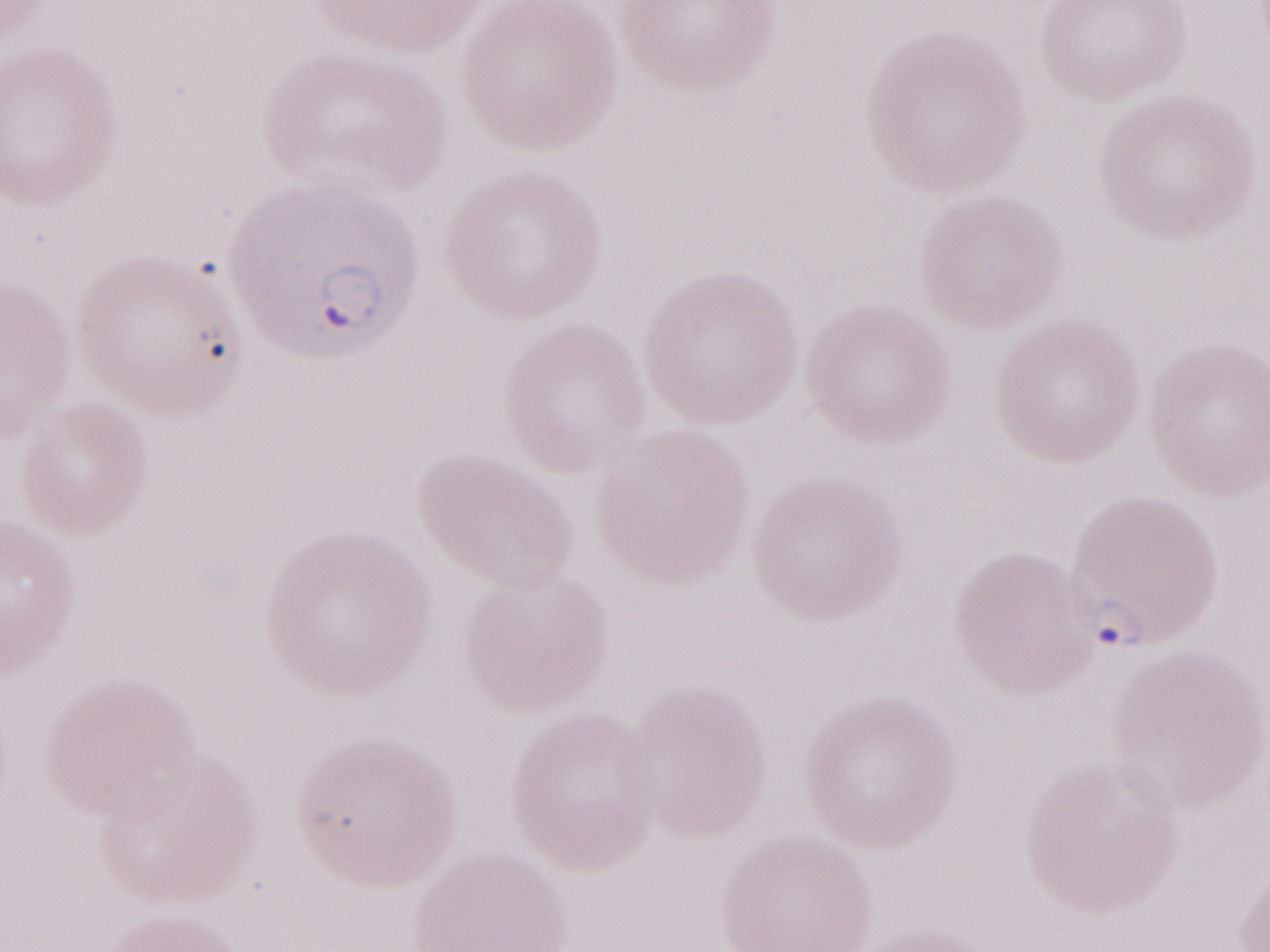 Thin peripheral-blood smear. Image is 1270×952 pixels. One field of this slide. Olympus BX43 microscope, Olympus DP73 camera. Magnification: 1,000x. Patient diagnosis: malaria infection. May-Grünwald-Giemsa stain.